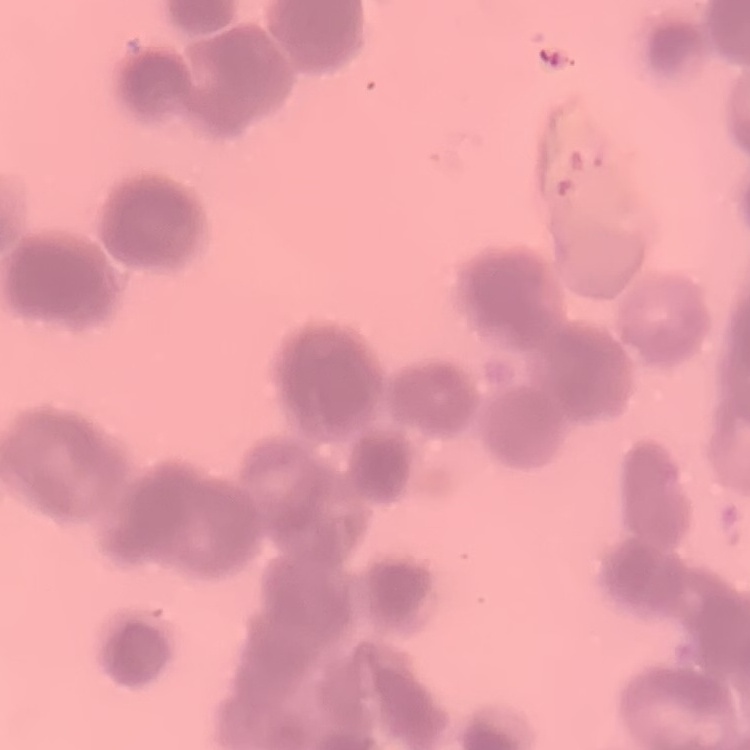
Summary:
  - Erythrocyte morphology: rouleaux formation
  - Stain: Field's or Giemsa
  - Preparation: thin blood smear
  - Image type: one tile cut from a larger photomicrograph